Classify this cell by malaria status.
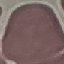

Uninfected.

Acquired by smartphone through the microscope eyepiece. Giemsa-stained preparation. Thin blood film. Automatically extracted cell patch, resized to 64 × 64 pixels.